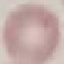

Malaria status: uninfected. Giemsa-stained preparation. Thin blood smear. Acquired by smartphone through the microscope eyepiece. Cell patch, automatically extracted from a larger field of view and resized to 64 × 64 pixels.